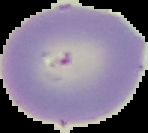

From a thin blood film. The area outside the segmented cell region is set to black. Image is 148×133 pixels. Result: no malaria parasites seen.